Name the parasite shown.
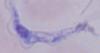

A trypanosome.

1000x magnification. Micrograph.